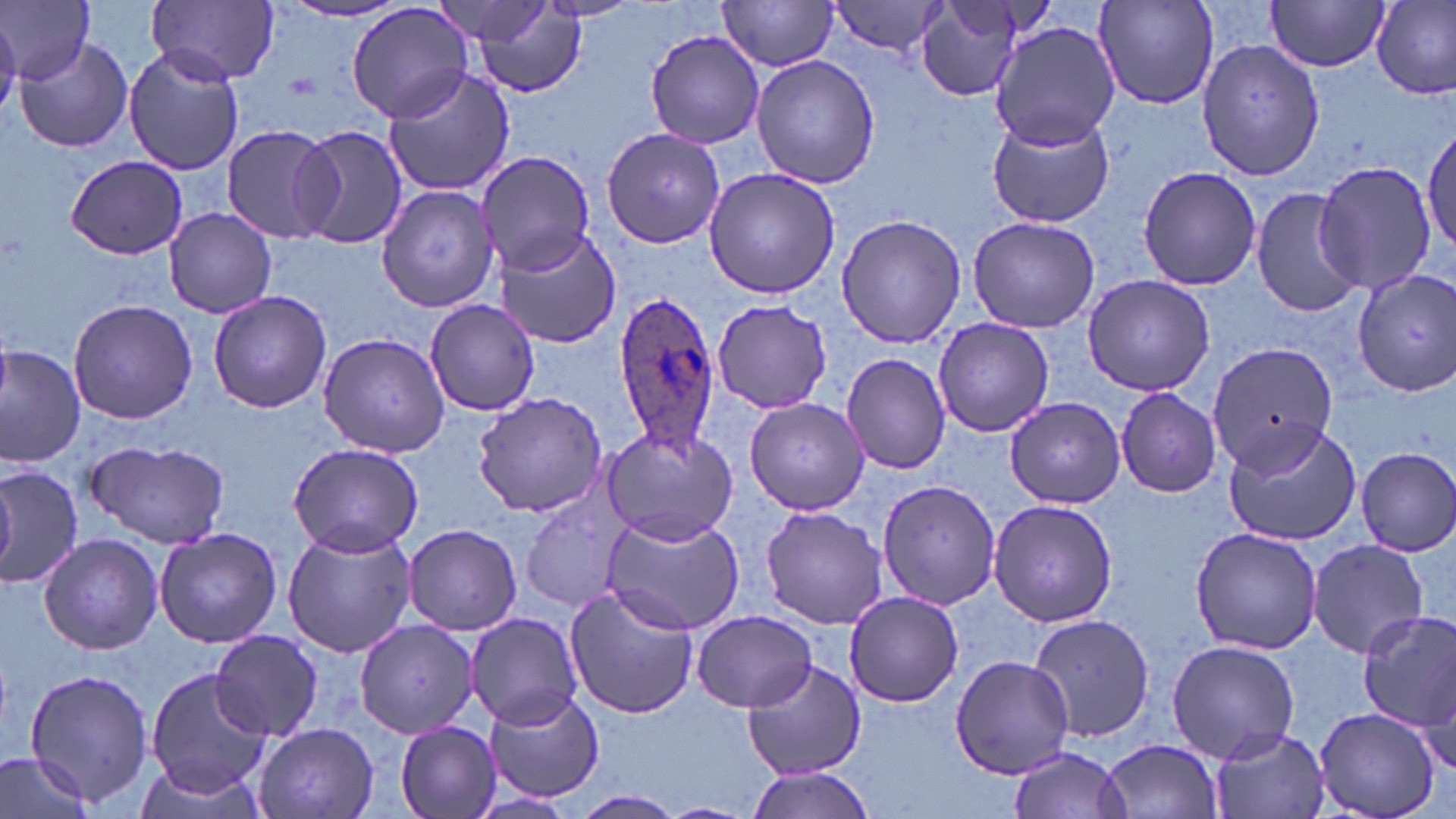
slide-level diagnosis = Plasmodium ovale
magnification = 1000x
Plasmodium ovale-infected red blood cell locations = approximate bounding boxes as (x1, y1, x2, y2) in pixels: (610, 288, 720, 456)
field of view = one of a larger specimen
stain = May-Grünwald-Giemsa
preparation = thin blood film
modality = optical microscopy
uninfected red blood cell locations = approximate bounding boxes as (x1, y1, x2, y2) in pixels: (1, 0, 95, 83), (148, 0, 281, 84), (544, 0, 640, 21), (1264, 0, 1391, 71), (717, 1, 840, 71), (831, 1, 952, 57), (1372, 1, 1456, 100), (279, 2, 408, 24), (345, 2, 476, 126), (431, 2, 559, 47), (915, 2, 1029, 102), (1093, 2, 1220, 109), (463, 3, 590, 100), (990, 22, 1123, 151), (644, 30, 766, 150), (16, 35, 134, 153), (1196, 35, 1325, 182), (123, 45, 245, 176), (752, 56, 879, 189), (384, 64, 515, 196), (987, 113, 1115, 229), (1422, 120, 1456, 261), (220, 123, 339, 244), (290, 124, 409, 250), (600, 126, 727, 247), (476, 151, 593, 275), (66, 155, 188, 260), (1313, 159, 1437, 297), (1136, 167, 1263, 292), (703, 168, 841, 299), (377, 185, 502, 313), (1252, 186, 1362, 317), (164, 208, 277, 318), (835, 213, 966, 349), (966, 214, 1100, 332), (490, 224, 622, 349), (1352, 268, 1455, 395), (1081, 274, 1215, 396), (208, 290, 332, 414), (68, 298, 197, 425), (425, 300, 541, 416), (710, 300, 831, 415), (933, 318, 1054, 437), (318, 332, 450, 458), (1205, 341, 1338, 469), (0, 346, 85, 466), (841, 352, 951, 474), (1115, 389, 1223, 497), (473, 392, 607, 517), (745, 396, 871, 517), (1004, 397, 1127, 509), (1222, 420, 1361, 546), (598, 424, 739, 545), (87, 441, 229, 548), (288, 442, 423, 557), (1355, 446, 1456, 556), (0, 461, 81, 590), (874, 474, 999, 615), (520, 489, 628, 612), (986, 497, 1120, 627), (761, 506, 888, 629), (603, 515, 744, 635), (403, 523, 522, 635), (283, 526, 414, 659), (154, 527, 282, 647), (1189, 527, 1321, 655), (38, 533, 162, 655), (1308, 538, 1431, 660), (562, 586, 698, 719), (844, 591, 963, 707), (691, 609, 817, 712), (1356, 610, 1456, 738), (1025, 611, 1157, 744), (466, 612, 584, 730), (354, 618, 481, 737), (210, 630, 324, 741), (1165, 638, 1301, 763), (950, 654, 1072, 778), (743, 659, 867, 780), (23, 666, 153, 805), (145, 667, 268, 795), (481, 686, 603, 801), (1312, 706, 1441, 819), (393, 719, 502, 819), (254, 722, 378, 819), (1206, 724, 1330, 819), (1100, 738, 1225, 818), (1005, 746, 1132, 819), (0, 752, 96, 819), (741, 770, 878, 819), (575, 790, 683, 817), (654, 802, 758, 819)
image size = 1456×819 pixels